Locate every blood parasite and identify its species.
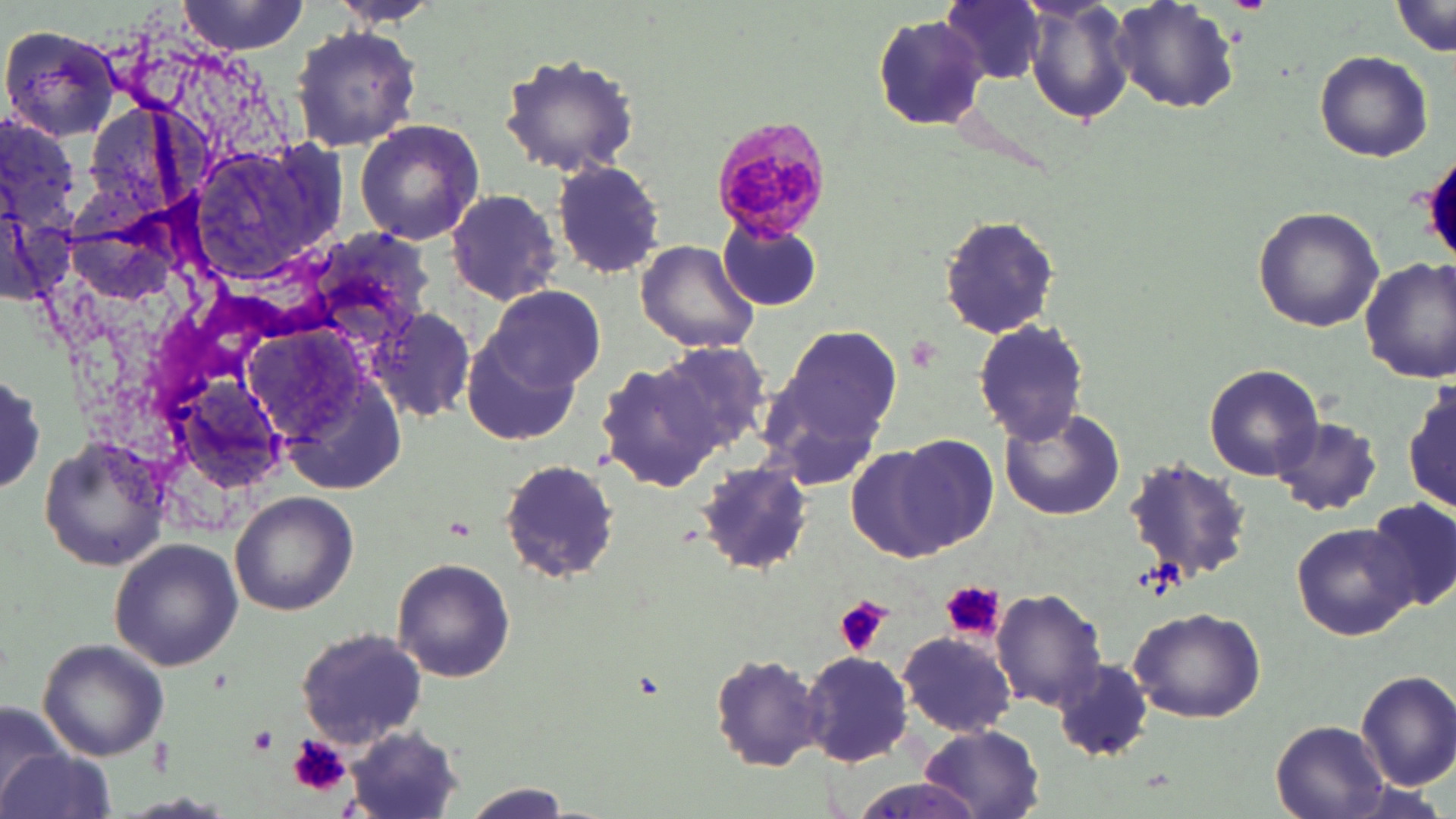
Approximate bounding boxes as [x1, y1, x2, y2] in pixels.
Plasmodium malariae-infected red blood cells: [711, 116, 835, 243].
No Plasmodium falciparum, Plasmodium ovale, Plasmodium vivax, Babesia divergens, or Trypanosoma brucei observed.

slide-level diagnosis = Plasmodium malariae
stain = May-Grünwald-Giemsa
platelet locations = approximate bounding boxes as [x1, y1, x2, y2] in pixels: [1229, 0, 1271, 11], [940, 578, 1004, 641], [835, 597, 891, 657], [247, 728, 277, 757], [290, 735, 351, 798]
modality = light microscopy
uninfected red blood cell locations = approximate bounding boxes as [x1, y1, x2, y2] in pixels: [177, 0, 312, 52], [940, 0, 1048, 86], [1022, 0, 1135, 126], [1109, 0, 1240, 113], [1390, 3, 1453, 58], [870, 14, 990, 132], [2, 24, 122, 142], [290, 24, 421, 152], [498, 50, 644, 178], [1315, 50, 1433, 163], [353, 117, 485, 247], [549, 159, 668, 281], [447, 188, 560, 304], [1251, 205, 1385, 332], [938, 215, 1059, 339], [716, 216, 824, 313], [634, 241, 760, 353], [1359, 255, 1455, 383], [486, 284, 605, 395], [371, 303, 476, 421], [973, 319, 1090, 445], [766, 321, 904, 457], [463, 326, 583, 445], [653, 340, 771, 453], [596, 359, 722, 494], [1204, 363, 1322, 480], [3, 366, 47, 497], [1405, 382, 1455, 516], [998, 405, 1126, 522], [1273, 417, 1383, 516], [37, 435, 170, 570], [899, 435, 1001, 549], [846, 443, 959, 561], [1123, 458, 1253, 583], [499, 460, 620, 583], [695, 463, 812, 578], [229, 491, 359, 617], [1364, 498, 1456, 610], [1291, 521, 1416, 641], [107, 535, 243, 672], [392, 556, 516, 684], [992, 588, 1106, 713], [1127, 605, 1267, 723], [295, 626, 428, 749], [898, 631, 1020, 738], [36, 637, 167, 761], [802, 650, 916, 768], [706, 651, 827, 772], [1056, 657, 1155, 761], [1354, 668, 1456, 790], [1, 701, 74, 813], [1270, 718, 1394, 818], [918, 724, 1045, 817], [344, 727, 468, 819], [1, 744, 116, 819], [841, 781, 994, 819], [457, 785, 578, 818]
field of view = one of a larger specimen
magnification = 1000x
image size = 1456×819 pixels
preparation = thin blood film